State which parasite is depicted.
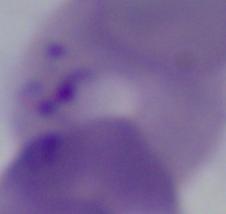
This is Babesia.

Captured at 1000x magnification. Micrograph.